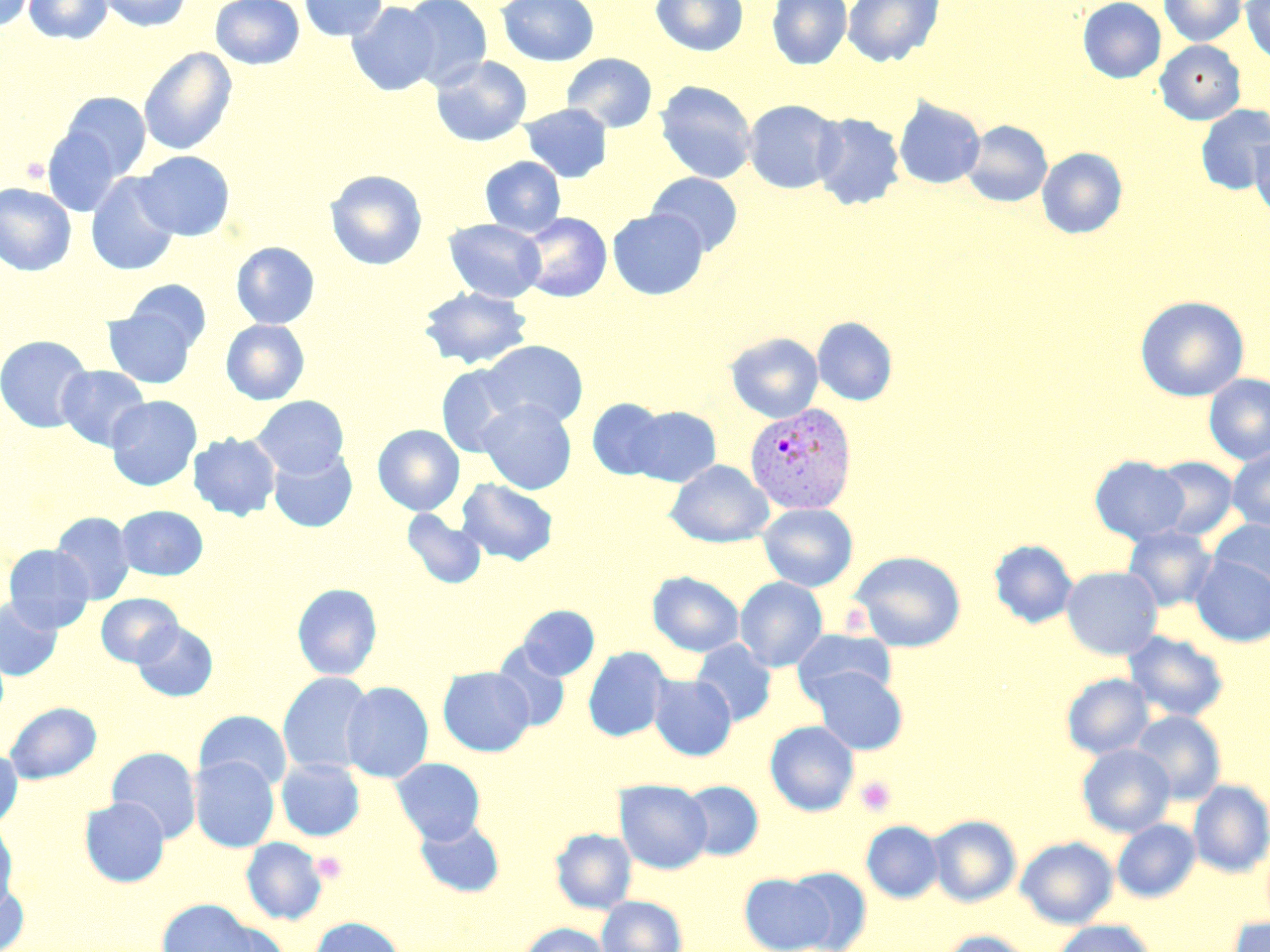
slide-level diagnosis = Plasmodium vivax
magnification = 1000x
stain = May-Grünwald-Giemsa
image size = 1270×952 pixels
Plasmodium vivax-infected red blood cell locations = approximate bounding boxes as (x1,y1)-(x2,y2) corner pairs in pixels: (744,402)-(857,515)
uninfected red blood cell locations = approximate bounding boxes as (x1,y1)-(x2,y2) corner pairs in pixels: (0,0)-(35,32), (24,0)-(113,44), (96,0)-(192,32), (210,0)-(304,70), (299,0)-(387,41), (399,0)-(492,90), (497,0)-(599,66), (651,0)-(748,56), (766,0)-(852,69), (842,0)-(944,66), (1078,0)-(1166,83), (1160,0)-(1246,46), (1241,0)-(1270,64), (347,2)-(440,97), (1155,39)-(1245,125), (138,47)-(237,156), (562,53)-(657,133), (430,55)-(532,147), (655,81)-(757,183), (57,91)-(151,183), (894,98)-(985,189), (743,99)-(843,194), (519,103)-(612,183), (1196,105)-(1270,194), (811,112)-(906,210), (962,120)-(1052,207), (41,126)-(129,217), (1250,134)-(1270,220), (1037,147)-(1128,239), (135,150)-(235,241), (480,156)-(566,237), (324,170)-(427,270), (647,172)-(743,256), (85,173)-(181,276), (0,183)-(76,276), (608,209)-(708,299), (517,212)-(611,302), (444,218)-(546,302), (231,242)-(320,329), (123,280)-(211,352), (419,286)-(533,369), (1135,296)-(1250,401), (103,308)-(198,388), (812,316)-(898,406), (220,319)-(310,405), (726,332)-(823,423), (0,334)-(93,433), (480,340)-(588,428), (56,365)-(150,450), (437,365)-(527,457), (1203,374)-(1270,466), (106,395)-(202,490), (252,395)-(349,478), (586,398)-(669,481), (477,399)-(577,494), (627,406)-(721,487), (373,424)-(464,515), (188,432)-(281,520), (268,448)-(357,532), (1227,448)-(1270,533), (1089,455)-(1190,544), (1149,455)-(1239,541), (666,460)-(774,547), (456,478)-(559,566), (758,503)-(858,592), (115,505)-(208,580), (402,509)-(487,589), (51,512)-(135,604), (1209,519)-(1270,597), (1122,525)-(1217,611), (989,539)-(1078,628), (3,544)-(95,633), (850,550)-(966,652), (1190,555)-(1270,647), (1061,566)-(1163,660), (647,571)-(744,656), (735,576)-(828,671), (292,583)-(383,680), (96,593)-(182,667), (0,597)-(62,680), (518,605)-(600,680), (132,620)-(218,701), (792,629)-(898,705), (1123,631)-(1229,722), (691,639)-(777,726), (492,642)-(571,732), (583,646)-(672,742), (808,666)-(908,755), (438,667)-(535,756), (278,672)-(375,777), (1061,673)-(1154,759), (649,674)-(737,760), (341,681)-(433,783), (5,702)-(101,784), (194,710)-(292,792), (1130,710)-(1226,804), (765,721)-(859,816), (1076,744)-(1175,837), (106,747)-(201,843), (0,748)-(23,829), (190,756)-(279,852), (276,758)-(365,841), (391,758)-(485,844), (614,779)-(712,874), (1188,779)-(1270,877), (679,780)-(763,860), (79,797)-(170,887), (928,814)-(1021,907), (415,816)-(505,898), (1113,819)-(1200,902), (0,820)-(19,917), (861,820)-(943,903), (550,828)-(637,914), (1016,836)-(1118,928), (241,837)-(327,925), (786,866)-(872,952), (740,873)-(834,951), (0,878)-(30,952), (596,896)-(687,952), (158,899)-(263,951), (1227,915)-(1270,952), (308,917)-(407,952), (1053,920)-(1155,952), (517,922)-(612,952), (939,930)-(1035,952)
field of view = single
modality = optical microscopy
preparation = thin blood film
platelet locations = approximate bounding boxes as (x1,y1)-(x2,y2) corner pairs in pixels: (855,776)-(896,816), (312,850)-(346,884)